Comment on the morphology of the erythrocytes.
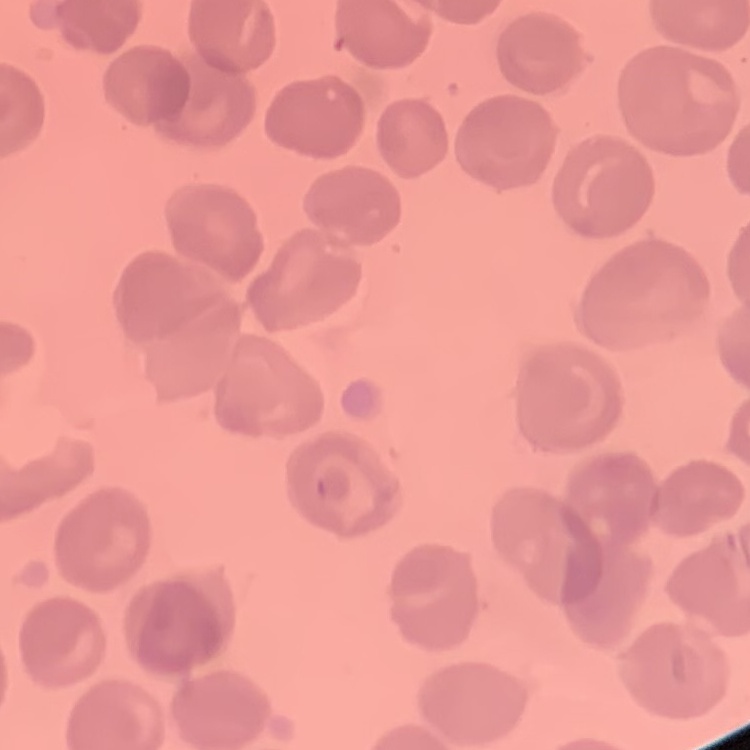

They show no rouleaux formation.

preparation = thin peripheral smear
stain = Field's or Giemsa
image type = one tile cut from a larger photomicrograph